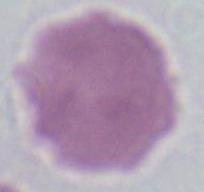

magnification = 1000x
identification = erythrocyte
modality = micrograph